Name the parasite shown.
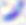

This is Toxoplasma gondii.

Summary:
  - Magnification: 400x
  - Modality: micrograph